Locate every Plasmodium ovale-infected red blood cell.
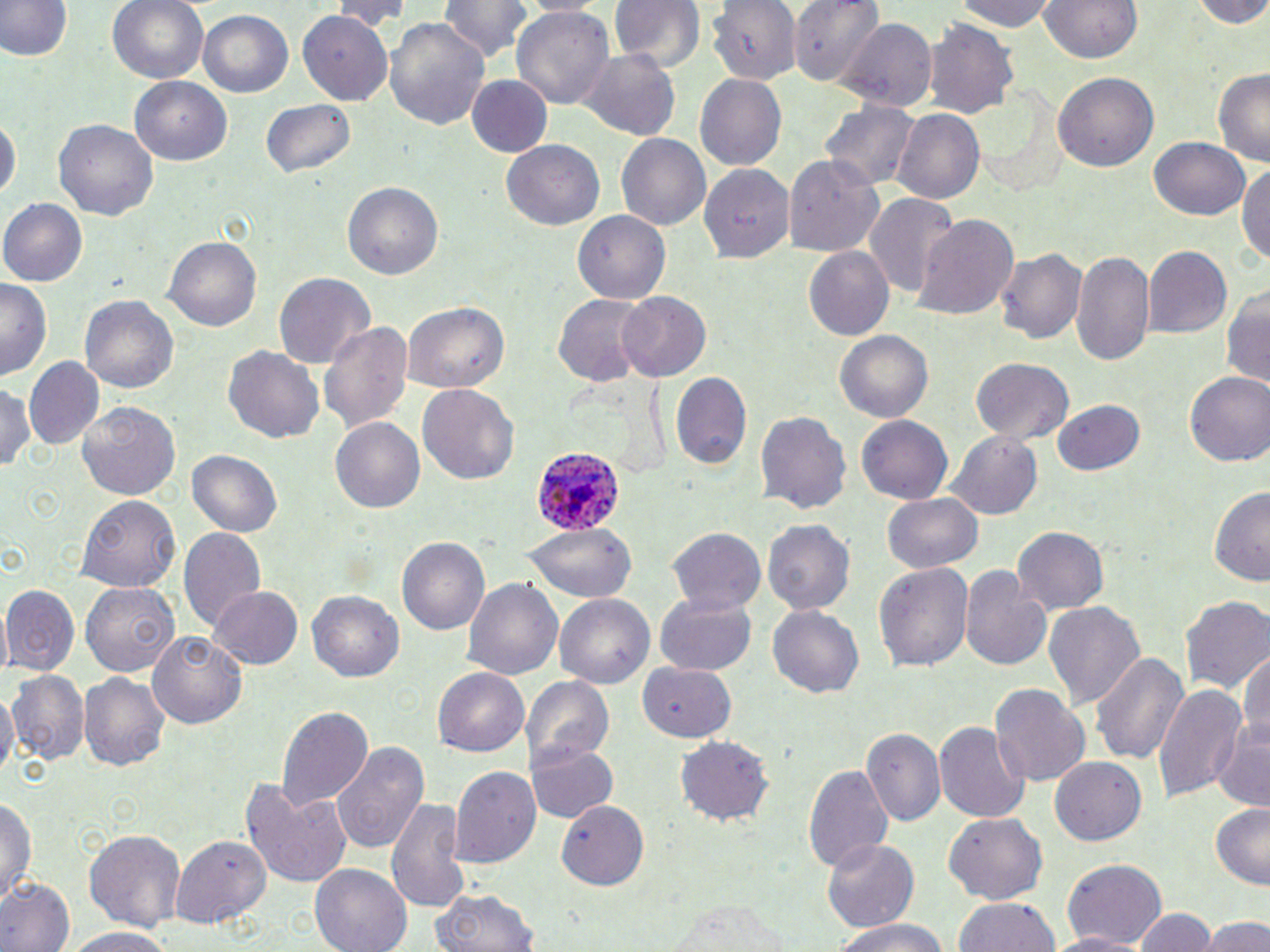
Approximate bounding boxes as [x1, y1, x2, y2] in pixels.
Plasmodium ovale-infected red blood cells: [531, 445, 623, 533].

slide_level_diagnosis: Plasmodium ovale
uninfected_red_blood_cell_locations: 'approximate bounding boxes as [x1, y1, x2, y2] in pixels: [1, 0, 72, 63], [107, 0, 211, 85], [330, 0, 412, 32], [436, 0, 536, 64], [611, 0, 703, 75], [707, 0, 803, 84], [790, 0, 884, 83], [951, 0, 1061, 30], [1044, 0, 1141, 64], [1181, 0, 1270, 26], [511, 5, 616, 114], [197, 9, 294, 99], [294, 10, 395, 107], [382, 14, 492, 136], [834, 17, 939, 112], [923, 21, 1017, 118], [575, 46, 681, 142], [1211, 69, 1270, 164], [1051, 72, 1156, 171], [693, 73, 786, 172], [468, 75, 552, 158], [131, 77, 231, 165], [261, 98, 357, 180], [819, 100, 920, 190], [893, 108, 985, 205], [1, 113, 18, 206], [53, 118, 158, 223], [614, 133, 711, 233], [1150, 135, 1253, 221], [501, 140, 604, 231], [783, 150, 884, 255], [1239, 158, 1270, 267], [704, 165, 797, 260], [342, 182, 443, 283], [864, 194, 958, 303], [0, 200, 85, 287], [575, 210, 671, 304], [912, 215, 1019, 322], [166, 237, 261, 331], [802, 246, 895, 343], [1143, 246, 1232, 340], [998, 248, 1086, 347], [1071, 250, 1153, 366], [273, 271, 375, 369], [1, 279, 50, 382], [1224, 285, 1269, 390], [551, 292, 649, 388], [614, 292, 712, 381], [80, 293, 178, 395], [401, 300, 508, 394], [317, 319, 412, 437], [835, 330, 933, 423], [224, 347, 324, 442], [969, 357, 1076, 444], [23, 358, 102, 448], [670, 371, 751, 472], [1184, 372, 1270, 468], [1, 382, 37, 476], [418, 384, 519, 485], [1053, 397, 1146, 475], [77, 400, 183, 500], [755, 411, 850, 515], [329, 417, 427, 514], [857, 417, 952, 501], [945, 430, 1045, 520], [186, 448, 283, 538], [1210, 485, 1270, 586], [882, 491, 983, 574], [76, 492, 182, 591], [761, 520, 854, 615], [524, 522, 636, 604], [1011, 525, 1109, 614], [177, 526, 266, 632], [670, 526, 765, 614], [396, 536, 491, 636], [873, 561, 974, 672], [962, 567, 1053, 671], [463, 577, 562, 685], [82, 580, 181, 675], [2, 585, 81, 674], [209, 587, 303, 670], [307, 590, 405, 681], [556, 593, 657, 689], [655, 594, 757, 675], [1181, 596, 1269, 695], [1043, 601, 1143, 710], [768, 603, 864, 697], [147, 631, 247, 729], [1089, 649, 1190, 767], [1238, 649, 1269, 753], [637, 662, 736, 742], [432, 667, 530, 758], [79, 670, 171, 772], [7, 671, 88, 766], [522, 676, 614, 765], [991, 684, 1090, 785], [1152, 684, 1247, 806], [0, 686, 17, 783], [277, 706, 372, 811], [935, 720, 1027, 824], [1212, 727, 1270, 811], [862, 728, 944, 825], [677, 737, 774, 825], [528, 740, 617, 825], [330, 742, 428, 855], [1052, 756, 1147, 846], [802, 760, 893, 873], [451, 765, 540, 870], [245, 778, 352, 888], [0, 793, 39, 903], [386, 795, 467, 915], [557, 797, 650, 889], [1209, 805, 1270, 888], [944, 813, 1048, 903], [83, 826, 188, 930], [171, 833, 269, 933], [821, 838, 917, 933], [1059, 857, 1167, 948], [310, 863, 412, 952], [0, 878, 74, 952], [429, 886, 539, 952], [953, 896, 1060, 952], [666, 898, 797, 950], [1132, 906, 1217, 952], [1202, 915, 1268, 952], [830, 918, 949, 952], [62, 927, 177, 951], [1044, 932, 1153, 952]'
preparation: thin blood smear
field_of_view: single
image_size: 1270×952 pixels
magnification: 1000x
stain: May-Grünwald-Giemsa
modality: light microscopy